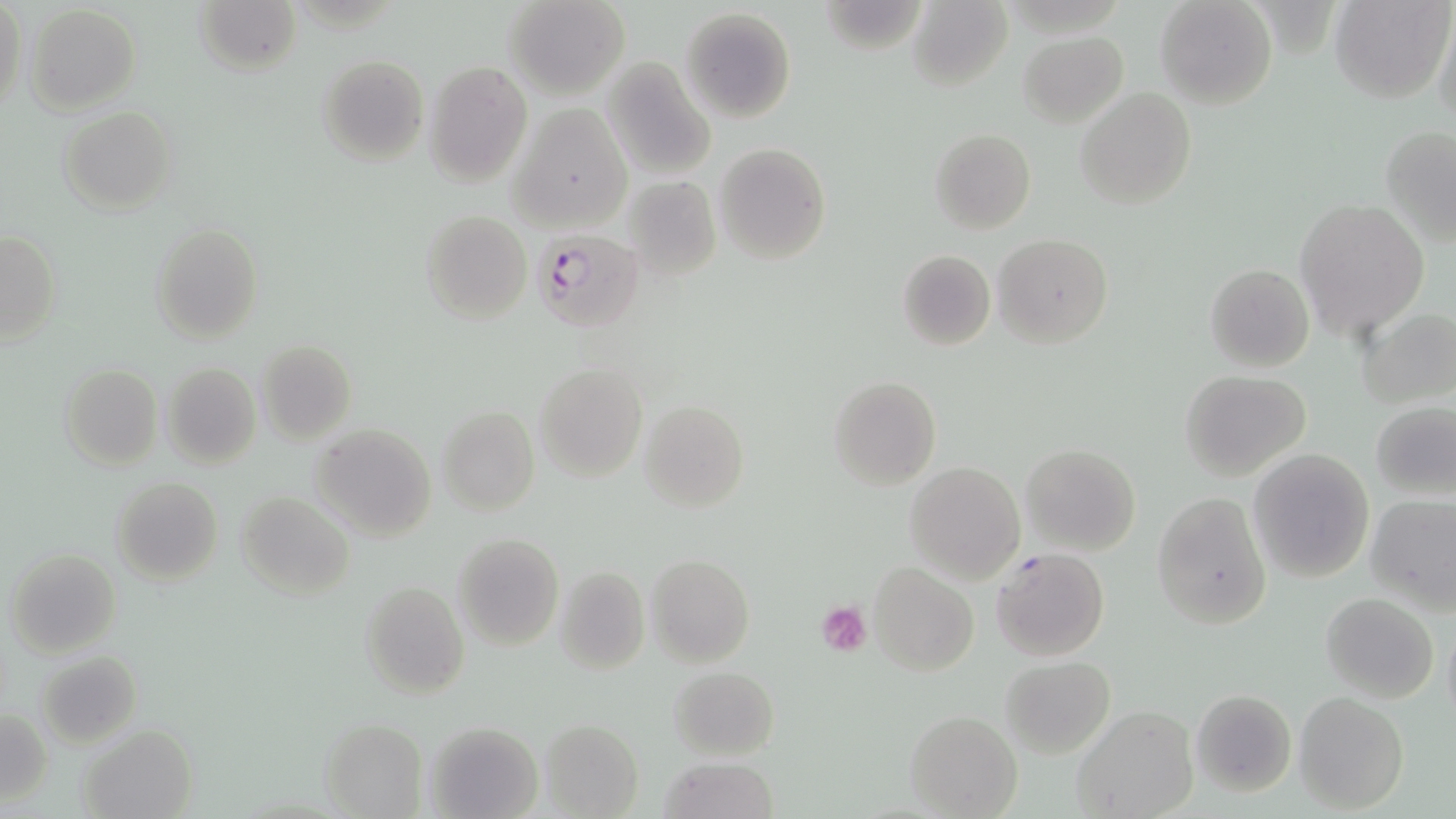

Summary:
  - Coordinate format: approximate bounding boxes as named x1/y1/x2/y2 corners in pixels
  - Uninfected red blood cell locations: (x1=195, y1=0, x2=301, y2=78), (x1=504, y1=0, x2=629, y2=100), (x1=1155, y1=0, x2=1277, y2=110), (x1=1329, y1=0, x2=1452, y2=104), (x1=0, y1=1, x2=25, y2=113), (x1=907, y1=1, x2=1013, y2=90), (x1=25, y1=4, x2=141, y2=115), (x1=680, y1=8, x2=797, y2=125), (x1=1433, y1=12, x2=1456, y2=132), (x1=1018, y1=32, x2=1129, y2=127), (x1=316, y1=53, x2=429, y2=165), (x1=602, y1=58, x2=717, y2=181), (x1=425, y1=61, x2=532, y2=185), (x1=1075, y1=88, x2=1196, y2=209), (x1=508, y1=104, x2=630, y2=232), (x1=59, y1=106, x2=176, y2=216), (x1=1379, y1=127, x2=1453, y2=240), (x1=930, y1=129, x2=1036, y2=236), (x1=714, y1=143, x2=831, y2=265), (x1=617, y1=177, x2=724, y2=281), (x1=1293, y1=199, x2=1429, y2=341), (x1=420, y1=210, x2=532, y2=324), (x1=152, y1=223, x2=262, y2=346), (x1=1, y1=230, x2=61, y2=345), (x1=993, y1=235, x2=1112, y2=349), (x1=896, y1=250, x2=996, y2=350), (x1=1205, y1=263, x2=1314, y2=372), (x1=1358, y1=307, x2=1455, y2=410), (x1=256, y1=340, x2=357, y2=444), (x1=160, y1=362, x2=261, y2=469), (x1=533, y1=363, x2=647, y2=482), (x1=60, y1=364, x2=162, y2=471), (x1=1180, y1=369, x2=1312, y2=480), (x1=828, y1=375, x2=941, y2=490), (x1=641, y1=400, x2=749, y2=514), (x1=1371, y1=401, x2=1456, y2=501), (x1=436, y1=405, x2=538, y2=516), (x1=310, y1=422, x2=437, y2=540), (x1=1019, y1=444, x2=1140, y2=555), (x1=1249, y1=448, x2=1375, y2=583), (x1=904, y1=458, x2=1022, y2=579), (x1=111, y1=476, x2=223, y2=586), (x1=235, y1=491, x2=355, y2=600), (x1=1151, y1=491, x2=1272, y2=629), (x1=1365, y1=493, x2=1456, y2=610), (x1=451, y1=534, x2=563, y2=652), (x1=6, y1=547, x2=121, y2=656), (x1=646, y1=554, x2=753, y2=668), (x1=869, y1=563, x2=978, y2=676), (x1=555, y1=565, x2=650, y2=676), (x1=360, y1=581, x2=468, y2=699), (x1=1320, y1=593, x2=1439, y2=704), (x1=1442, y1=620, x2=1456, y2=731), (x1=36, y1=652, x2=142, y2=747), (x1=1000, y1=655, x2=1115, y2=759), (x1=668, y1=666, x2=778, y2=760), (x1=1190, y1=689, x2=1297, y2=797), (x1=1295, y1=691, x2=1408, y2=814), (x1=1073, y1=704, x2=1199, y2=819), (x1=2, y1=709, x2=51, y2=806), (x1=905, y1=710, x2=1023, y2=818), (x1=320, y1=719, x2=426, y2=816), (x1=541, y1=720, x2=643, y2=816), (x1=426, y1=722, x2=541, y2=818), (x1=80, y1=724, x2=198, y2=818), (x1=658, y1=756, x2=781, y2=818)
  - Plasmodium falciparum-infected red blood cell locations: (x1=534, y1=227, x2=647, y2=333), (x1=991, y1=548, x2=1110, y2=661)
  - Platelet locations: (x1=816, y1=600, x2=872, y2=655)
  - Slide-level diagnosis: Plasmodium falciparum
  - Stain: May-Grünwald-Giemsa
  - Magnification: 1000x
  - Preparation: thin blood film
  - Field of view: single
  - Modality: optical microscopy
  - Image size: 1456×819 pixels